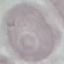
Summary:
  - Malaria status: uninfected
  - Preparation: thin blood film
  - Image type: automatically extracted cell patch, resized to 64 × 64 pixels
  - Capture: smartphone through the microscope eyepiece
  - Stain: Giemsa